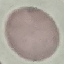

Malaria status: uninfected. Giemsa-stained preparation. Photographed with a smartphone camera at the microscope eyepiece. Thin smear of blood. Automatically extracted cell patch, resized to 64 × 64 pixels.